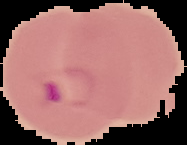
Image is 187×145 pixels. From a thin blood smear. Cell region segmented out of the field of view; the surrounding area is masked to black. Malaria status: parasitized.